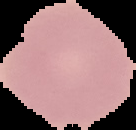

Summary:
  - Image size: 136×130 pixels
  - Malaria status: uninfected
  - Preparation: thin blood smear
  - Image type: segmented cell region on a black background